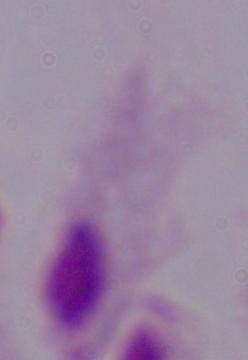

magnification: 1000x
identification: trichomonad
modality: photomicrograph